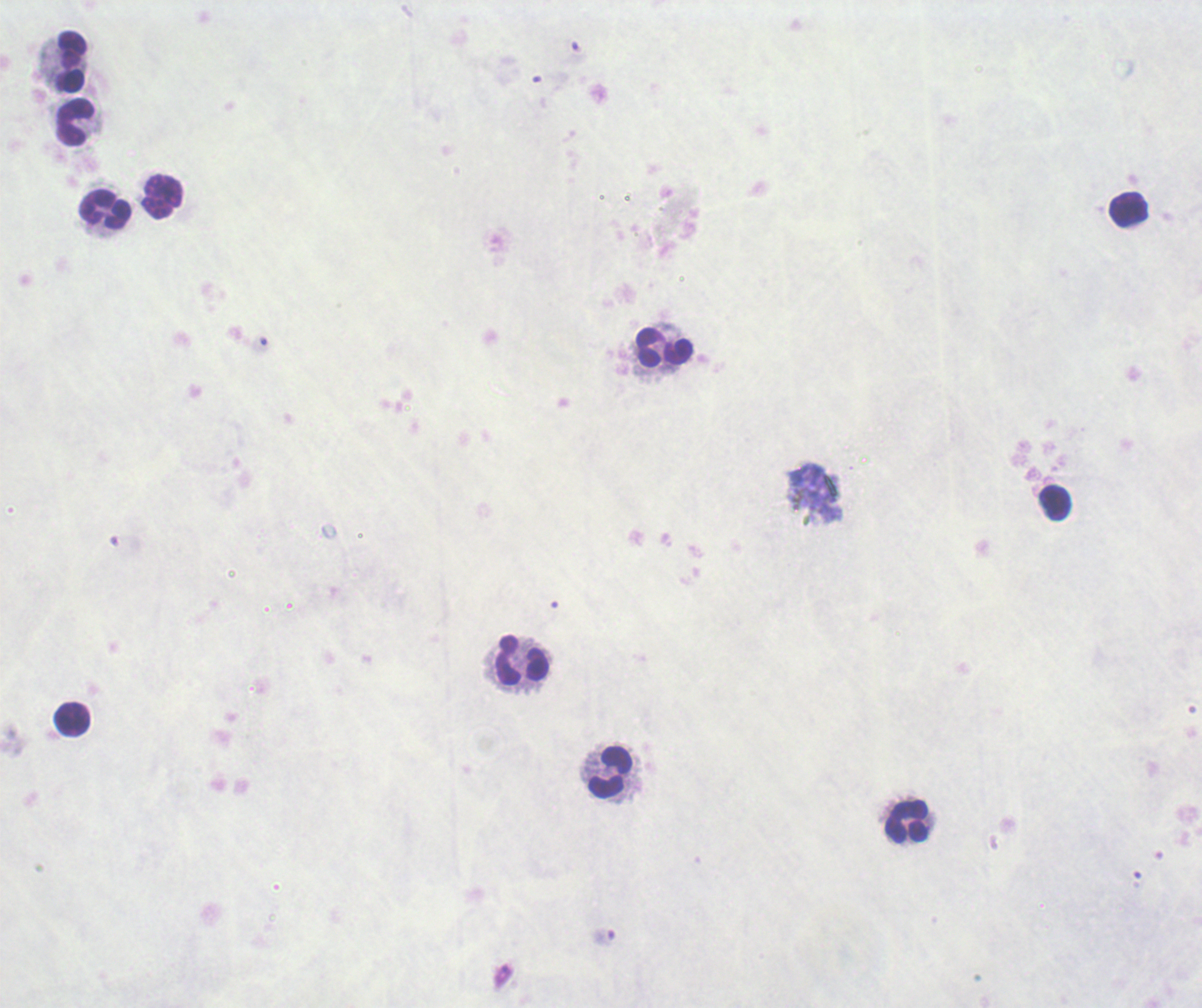
Approximate centers as (x, y) in pixels. Leukocyte locations: (70, 62), (76, 123), (161, 197), (104, 210), (1128, 210), (663, 347), (1054, 502), (521, 661), (72, 719), (610, 772), (907, 821). Background quality: unsatisfactory. Romanowsky-stained preparation. Image is 1202×1008 pixels. 100x magnification. One field from this slide. Previously used in an actual diagnosis. Result: no Plasmodium parasites seen. Thick smear of blood.